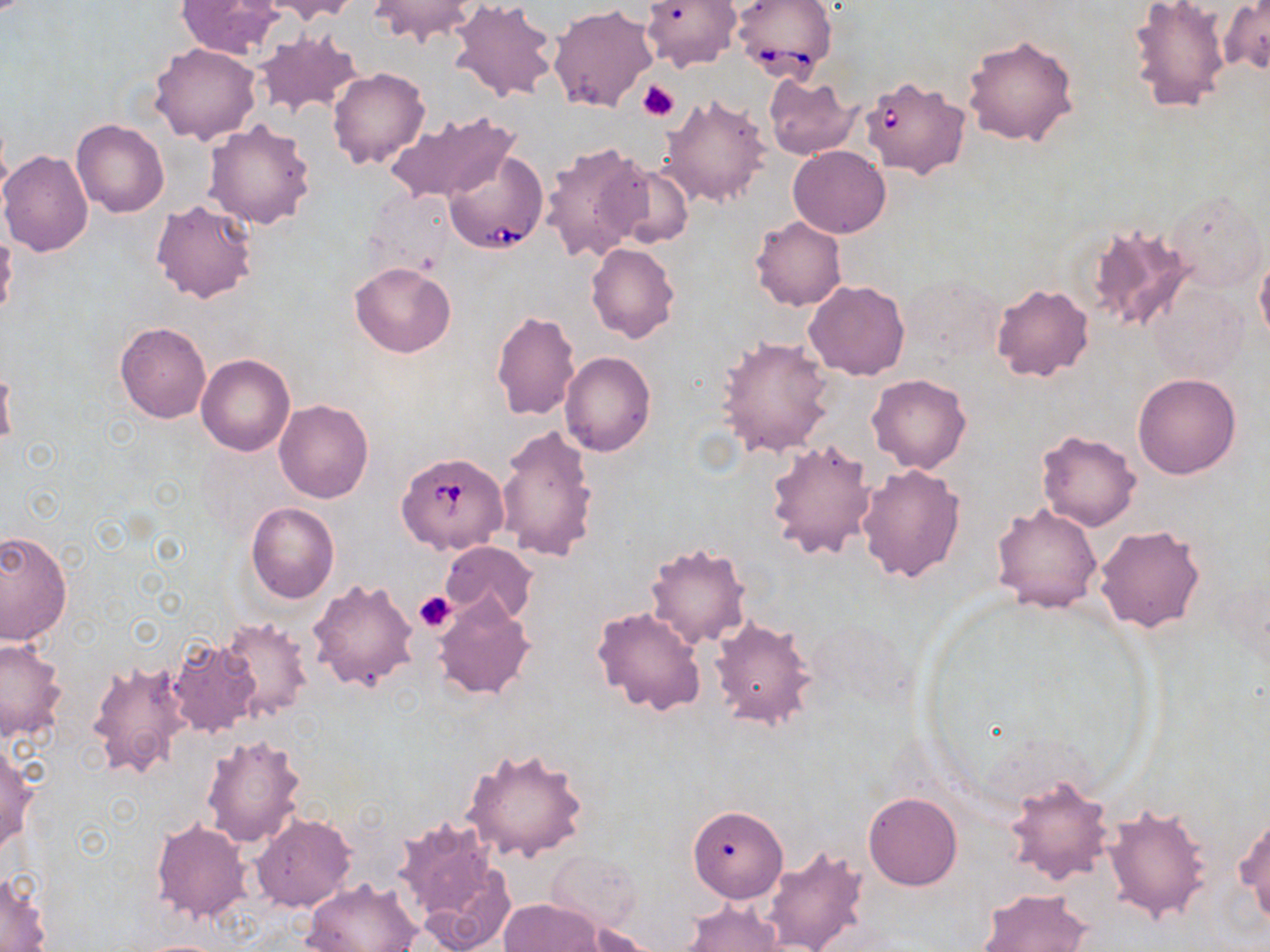

Approximate bounding boxes as named x1/y1/x2/y2 corners in pixels. Platelet locations: (x1=638, y1=80, x2=679, y2=121), (x1=414, y1=591, x2=455, y2=633). Uninfected red blood cell locations: (x1=174, y1=0, x2=283, y2=60), (x1=263, y1=0, x2=359, y2=22), (x1=369, y1=0, x2=479, y2=47), (x1=448, y1=0, x2=559, y2=104), (x1=1126, y1=0, x2=1233, y2=115), (x1=642, y1=1, x2=740, y2=72), (x1=1219, y1=2, x2=1269, y2=76), (x1=548, y1=4, x2=657, y2=112), (x1=253, y1=30, x2=364, y2=118), (x1=962, y1=32, x2=1079, y2=147), (x1=150, y1=43, x2=260, y2=144), (x1=327, y1=68, x2=430, y2=170), (x1=764, y1=74, x2=860, y2=159), (x1=660, y1=92, x2=770, y2=209), (x1=385, y1=111, x2=518, y2=205), (x1=204, y1=118, x2=316, y2=228), (x1=72, y1=119, x2=169, y2=218), (x1=7, y1=132, x2=162, y2=232), (x1=540, y1=140, x2=652, y2=264), (x1=789, y1=145, x2=891, y2=238), (x1=0, y1=149, x2=93, y2=256), (x1=605, y1=161, x2=695, y2=250), (x1=366, y1=187, x2=454, y2=275), (x1=1164, y1=187, x2=1266, y2=293), (x1=150, y1=200, x2=258, y2=303), (x1=750, y1=216, x2=847, y2=311), (x1=1084, y1=222, x2=1198, y2=334), (x1=586, y1=243, x2=679, y2=343), (x1=1254, y1=253, x2=1270, y2=348), (x1=349, y1=263, x2=456, y2=358), (x1=803, y1=280, x2=910, y2=381), (x1=991, y1=282, x2=1094, y2=381), (x1=1146, y1=282, x2=1249, y2=385), (x1=492, y1=310, x2=579, y2=421), (x1=114, y1=321, x2=212, y2=424), (x1=716, y1=335, x2=834, y2=458), (x1=560, y1=352, x2=656, y2=457), (x1=196, y1=354, x2=295, y2=456), (x1=0, y1=365, x2=16, y2=448), (x1=1132, y1=372, x2=1241, y2=478), (x1=868, y1=374, x2=970, y2=473), (x1=274, y1=399, x2=374, y2=503), (x1=496, y1=423, x2=600, y2=563), (x1=1035, y1=429, x2=1141, y2=532), (x1=765, y1=438, x2=878, y2=562), (x1=856, y1=464, x2=966, y2=583), (x1=245, y1=502, x2=338, y2=603), (x1=992, y1=503, x2=1102, y2=613), (x1=1094, y1=523, x2=1207, y2=635), (x1=0, y1=529, x2=72, y2=647), (x1=439, y1=541, x2=538, y2=626), (x1=644, y1=543, x2=750, y2=649), (x1=308, y1=577, x2=420, y2=692), (x1=433, y1=594, x2=535, y2=703), (x1=592, y1=606, x2=705, y2=716), (x1=216, y1=616, x2=312, y2=721), (x1=710, y1=616, x2=821, y2=732), (x1=166, y1=636, x2=262, y2=737), (x1=0, y1=637, x2=66, y2=743), (x1=86, y1=658, x2=193, y2=780), (x1=201, y1=734, x2=307, y2=849), (x1=0, y1=742, x2=35, y2=852), (x1=461, y1=744, x2=591, y2=863), (x1=1002, y1=774, x2=1114, y2=887), (x1=863, y1=791, x2=962, y2=890), (x1=1102, y1=804, x2=1213, y2=924), (x1=690, y1=806, x2=787, y2=902), (x1=1236, y1=811, x2=1270, y2=927), (x1=251, y1=813, x2=356, y2=912), (x1=394, y1=817, x2=505, y2=936), (x1=150, y1=820, x2=251, y2=921), (x1=760, y1=843, x2=868, y2=952), (x1=547, y1=850, x2=642, y2=933), (x1=1, y1=871, x2=52, y2=951), (x1=302, y1=877, x2=421, y2=952), (x1=976, y1=888, x2=1093, y2=952), (x1=499, y1=898, x2=601, y2=951), (x1=680, y1=901, x2=786, y2=951), (x1=573, y1=923, x2=659, y2=952). Babesia divergens-infected red blood cell locations: (x1=730, y1=0, x2=836, y2=82), (x1=860, y1=75, x2=971, y2=179), (x1=444, y1=148, x2=549, y2=256), (x1=398, y1=451, x2=508, y2=555). Slide-level diagnosis: Babesia divergens. Captured at 1000x magnification. May-Grünwald-Giemsa-stained preparation. Image is 1270×952 pixels. Light microscopy. Single field of view. Thin blood film.